Locate every Plasmodium ovale-infected red blood cell.
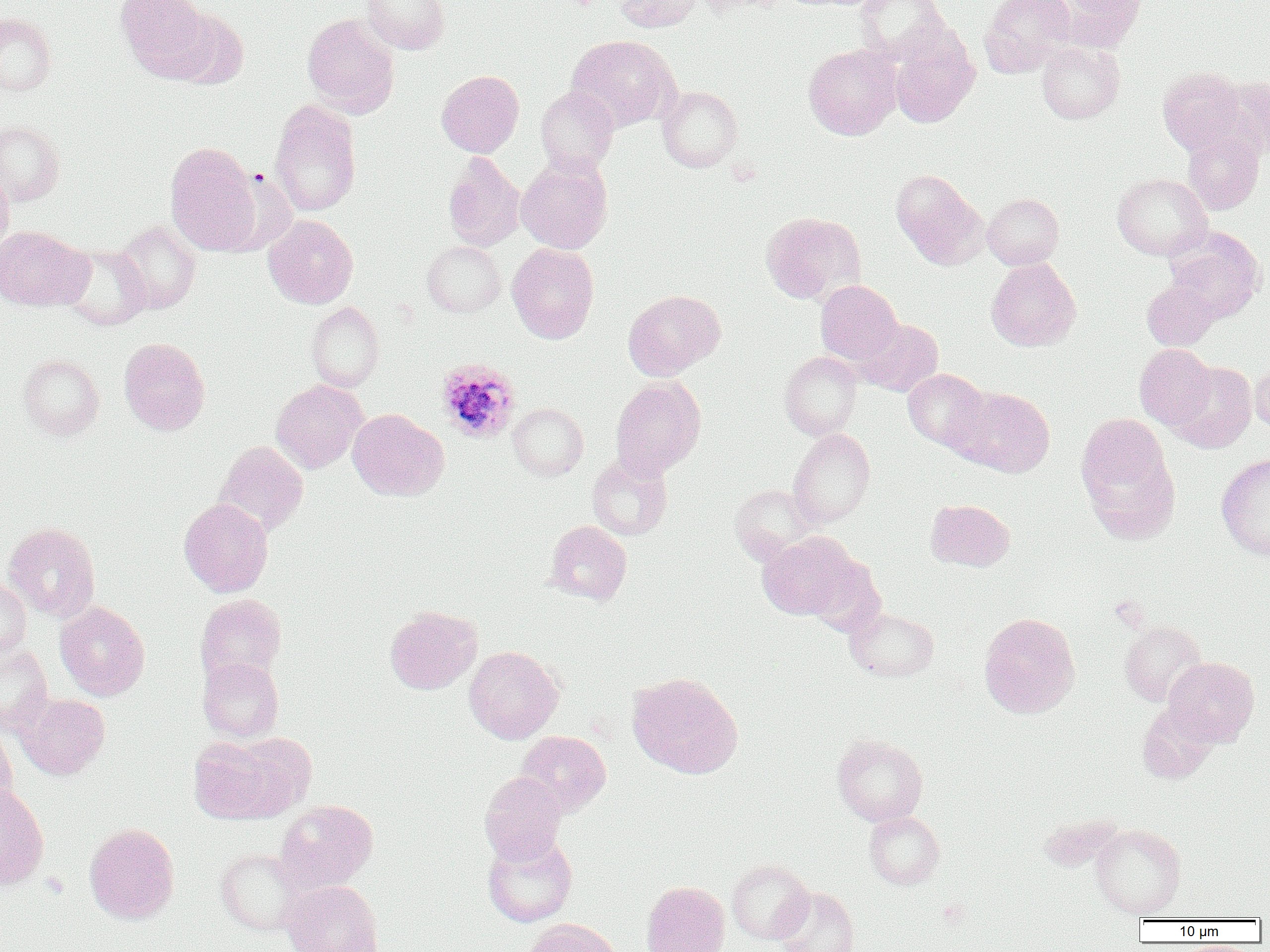

Approximate bounding boxes as named x1/y1/x2/y2 corners in pixels.
Plasmodium ovale-infected red blood cells: (x1=435, y1=358, x2=521, y2=443).

Uninfected red blood cell locations: (x1=115, y1=0, x2=211, y2=79), (x1=360, y1=0, x2=450, y2=54), (x1=615, y1=0, x2=701, y2=32), (x1=696, y1=0, x2=785, y2=14), (x1=855, y1=0, x2=948, y2=63), (x1=980, y1=0, x2=1076, y2=76), (x1=1060, y1=0, x2=1147, y2=47), (x1=165, y1=8, x2=249, y2=89), (x1=0, y1=12, x2=56, y2=96), (x1=302, y1=14, x2=399, y2=117), (x1=890, y1=31, x2=979, y2=128), (x1=566, y1=35, x2=679, y2=132), (x1=1036, y1=41, x2=1125, y2=123), (x1=804, y1=44, x2=902, y2=140), (x1=1157, y1=67, x2=1248, y2=155), (x1=436, y1=70, x2=524, y2=157), (x1=1219, y1=76, x2=1270, y2=158), (x1=657, y1=85, x2=743, y2=171), (x1=535, y1=86, x2=619, y2=174), (x1=270, y1=100, x2=361, y2=218), (x1=0, y1=122, x2=65, y2=206), (x1=1181, y1=126, x2=1265, y2=215), (x1=164, y1=141, x2=261, y2=255), (x1=442, y1=153, x2=524, y2=252), (x1=516, y1=156, x2=613, y2=254), (x1=0, y1=169, x2=14, y2=255), (x1=891, y1=169, x2=987, y2=269), (x1=1112, y1=173, x2=1212, y2=260), (x1=982, y1=193, x2=1064, y2=270), (x1=760, y1=211, x2=864, y2=304), (x1=263, y1=215, x2=358, y2=309), (x1=113, y1=220, x2=202, y2=314), (x1=0, y1=225, x2=91, y2=311), (x1=1164, y1=228, x2=1265, y2=321), (x1=422, y1=241, x2=506, y2=317), (x1=58, y1=243, x2=151, y2=331), (x1=507, y1=243, x2=599, y2=343), (x1=986, y1=258, x2=1081, y2=351), (x1=815, y1=280, x2=903, y2=365), (x1=1142, y1=280, x2=1219, y2=350), (x1=624, y1=289, x2=725, y2=379), (x1=305, y1=301, x2=384, y2=392), (x1=856, y1=318, x2=943, y2=396), (x1=119, y1=337, x2=210, y2=435), (x1=1134, y1=344, x2=1215, y2=430), (x1=779, y1=351, x2=862, y2=440), (x1=18, y1=354, x2=104, y2=440), (x1=1249, y1=359, x2=1270, y2=437), (x1=1170, y1=362, x2=1256, y2=453), (x1=903, y1=369, x2=991, y2=452), (x1=610, y1=376, x2=706, y2=478), (x1=270, y1=380, x2=366, y2=473), (x1=950, y1=386, x2=1056, y2=477), (x1=508, y1=403, x2=588, y2=481), (x1=348, y1=409, x2=447, y2=501), (x1=1076, y1=415, x2=1177, y2=537), (x1=789, y1=428, x2=875, y2=527), (x1=214, y1=441, x2=308, y2=535), (x1=586, y1=453, x2=672, y2=541), (x1=1216, y1=453, x2=1270, y2=560), (x1=730, y1=484, x2=820, y2=564), (x1=179, y1=499, x2=273, y2=597), (x1=926, y1=499, x2=1015, y2=571), (x1=546, y1=520, x2=632, y2=605), (x1=2, y1=522, x2=101, y2=622), (x1=759, y1=532, x2=860, y2=620), (x1=0, y1=574, x2=31, y2=660), (x1=195, y1=594, x2=286, y2=684), (x1=55, y1=602, x2=150, y2=700), (x1=384, y1=606, x2=482, y2=694), (x1=846, y1=606, x2=939, y2=682), (x1=979, y1=612, x2=1081, y2=718), (x1=1118, y1=620, x2=1206, y2=706), (x1=0, y1=643, x2=53, y2=735), (x1=464, y1=646, x2=563, y2=743), (x1=1164, y1=656, x2=1259, y2=746), (x1=198, y1=657, x2=284, y2=743), (x1=627, y1=672, x2=743, y2=778), (x1=15, y1=692, x2=110, y2=780), (x1=1137, y1=702, x2=1219, y2=783), (x1=0, y1=725, x2=17, y2=817), (x1=516, y1=730, x2=611, y2=815), (x1=222, y1=733, x2=316, y2=819), (x1=832, y1=734, x2=927, y2=826), (x1=188, y1=737, x2=282, y2=824), (x1=479, y1=771, x2=567, y2=865), (x1=0, y1=783, x2=49, y2=891), (x1=274, y1=800, x2=377, y2=892), (x1=864, y1=811, x2=945, y2=889), (x1=84, y1=823, x2=180, y2=924), (x1=1091, y1=823, x2=1186, y2=918), (x1=482, y1=834, x2=578, y2=927), (x1=216, y1=848, x2=306, y2=937), (x1=726, y1=859, x2=813, y2=944), (x1=281, y1=879, x2=383, y2=952), (x1=641, y1=881, x2=730, y2=952), (x1=774, y1=886, x2=860, y2=952), (x1=522, y1=919, x2=621, y2=952). Slide-level diagnosis: Plasmodium ovale. Single field of view. Thin blood film. Image is 1270×952 pixels. 1000x magnification. Light microscopy.